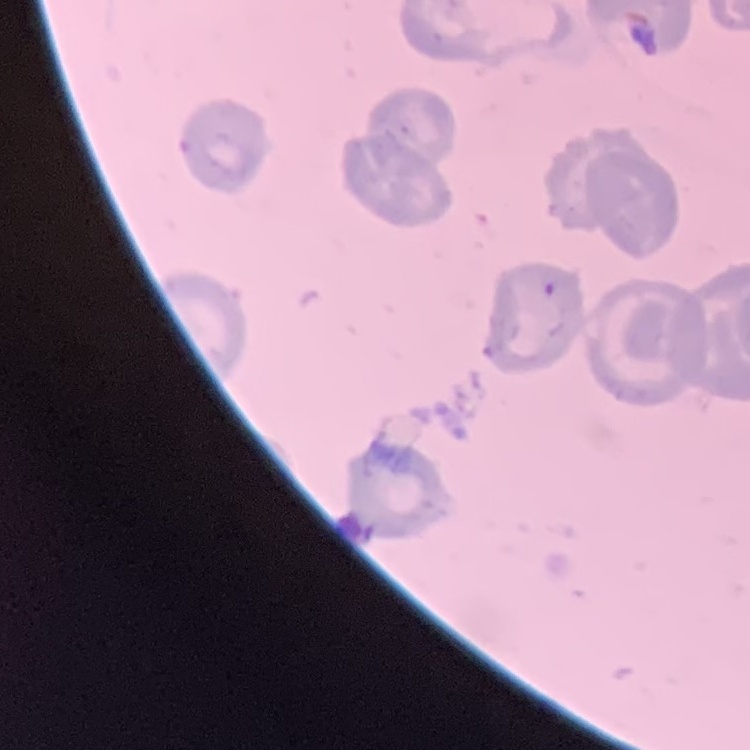
red blood cell morphology = no rouleaux formation
stain = Field's or Giemsa
preparation = thin peripheral smear
image type = square crop of a larger photomicrograph